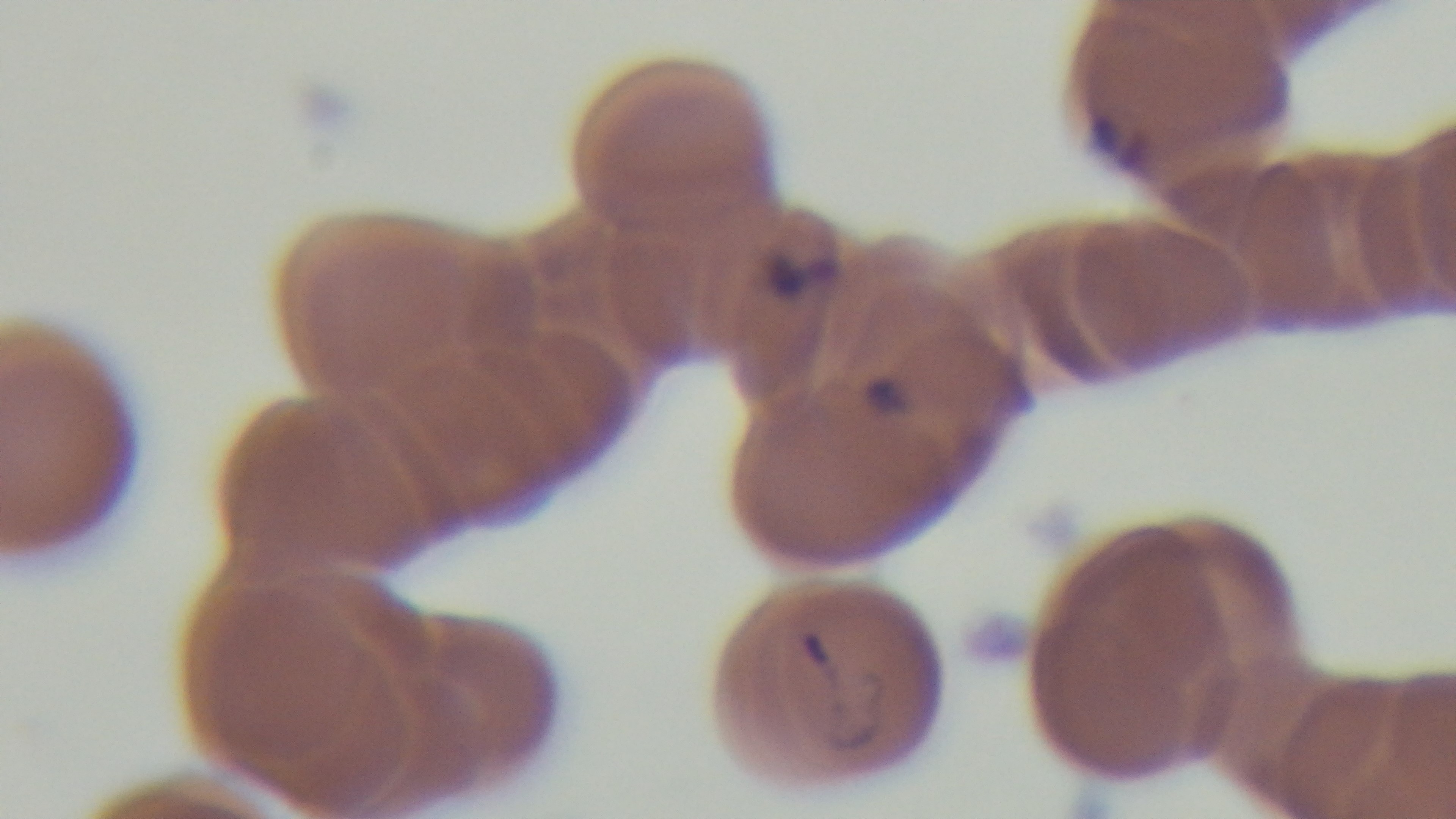

stain = Giemsa
preparation = thin
malaria status = positive
modality = light microscopy
field of view = single
objective = 100x oil immersion
capture = mounted 4K digital camera